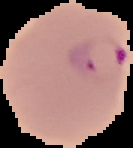
Summary:
  - Image type: cell region segmented out of the field of view; surrounding area masked to black
  - Preparation: thin blood smear
  - Image size: 133×148 pixels
  - Result: Plasmodium parasites identified